Classify this cell by malaria status.
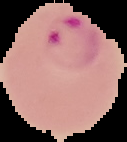
Parasitized.

preparation: thin blood smear
image_type: cell region segmented out of the field of view; surrounding area masked to black
image_size: 127×142 pixels